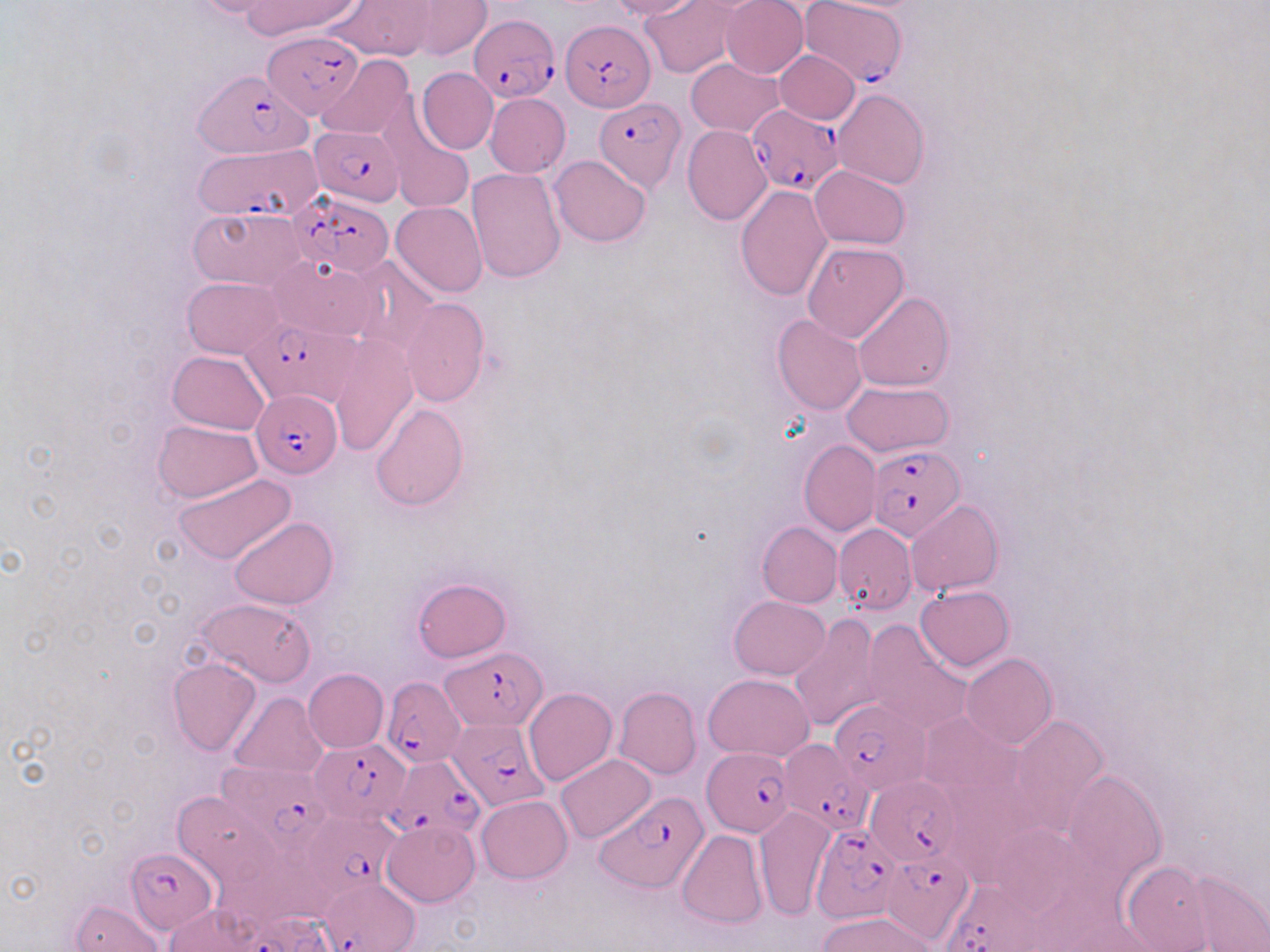

slide-level diagnosis = Plasmodium falciparum
preparation = thin blood film
uninfected red blood cell locations = approximate bounding boxes as [x1, y1, x2, y2] in pixels: [186, 0, 289, 18], [242, 0, 359, 40], [327, 0, 434, 61], [607, 0, 699, 20], [641, 0, 739, 77], [721, 0, 808, 78], [405, 1, 490, 59], [772, 49, 860, 123], [316, 55, 416, 139], [686, 58, 783, 137], [416, 68, 498, 154], [832, 88, 929, 189], [485, 93, 570, 177], [378, 100, 473, 216], [683, 125, 771, 225], [549, 155, 650, 248], [810, 166, 909, 250], [466, 168, 566, 284], [736, 186, 832, 300], [391, 202, 487, 299], [189, 205, 307, 290], [802, 242, 908, 343], [267, 256, 380, 342], [347, 256, 441, 357], [183, 277, 285, 357], [853, 293, 952, 392], [399, 299, 491, 406], [773, 314, 867, 414], [327, 336, 418, 457], [168, 350, 269, 435], [841, 381, 954, 455], [369, 403, 468, 509], [153, 419, 262, 502], [799, 440, 880, 536], [173, 472, 295, 566], [906, 500, 1003, 598], [229, 517, 337, 609], [757, 522, 842, 607], [833, 523, 916, 615], [413, 578, 511, 662], [915, 584, 1014, 671], [729, 595, 830, 678], [193, 596, 318, 688], [791, 614, 883, 731], [860, 621, 971, 733], [962, 653, 1057, 749], [168, 657, 261, 755], [303, 668, 388, 753], [703, 673, 814, 760], [524, 687, 617, 786], [614, 687, 701, 780], [230, 693, 330, 781], [916, 711, 1021, 803], [1010, 714, 1108, 833], [556, 753, 657, 843], [1060, 768, 1168, 888], [168, 789, 284, 895], [477, 795, 572, 883], [754, 806, 837, 921], [382, 819, 480, 907], [677, 828, 768, 929], [1119, 861, 1218, 950], [1166, 865, 1270, 952], [71, 899, 165, 951], [164, 904, 264, 952], [818, 912, 940, 951]
magnification = 1000x
Plasmodium falciparum-infected red blood cell locations = approximate bounding boxes as [x1, y1, x2, y2] in pixels: [798, 0, 909, 87], [472, 14, 558, 100], [561, 19, 655, 114], [262, 30, 361, 118], [200, 67, 316, 159], [594, 97, 686, 192], [747, 103, 842, 197], [309, 126, 405, 205], [193, 144, 322, 222], [289, 190, 395, 276], [245, 317, 355, 405], [254, 389, 342, 478], [866, 445, 964, 541], [444, 646, 546, 731], [381, 677, 464, 768], [830, 698, 930, 793], [448, 719, 551, 809], [311, 738, 410, 828], [778, 738, 875, 834], [701, 746, 795, 836], [389, 751, 482, 843], [219, 761, 331, 852], [867, 777, 958, 862], [598, 792, 709, 893], [298, 815, 400, 899], [808, 823, 905, 924], [125, 847, 219, 932], [880, 850, 974, 944], [323, 875, 419, 952], [938, 880, 1044, 952]
image size = 1270×952 pixels
modality = light microscopy
field of view = single
stain = May-Grünwald-Giemsa